Describe the morphology of the erythrocytes.
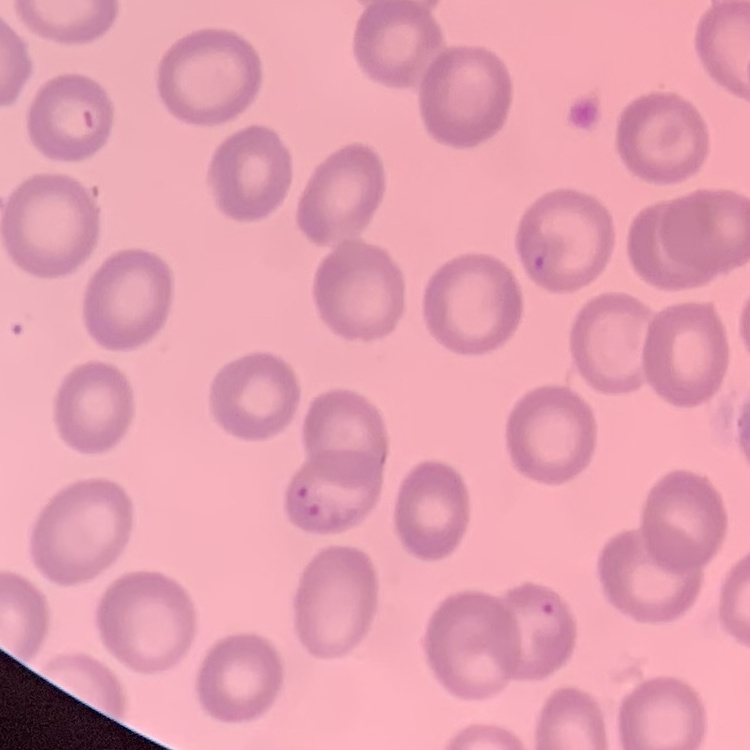
They show no rouleaux formation.

Thin blood smear. One tile cut from a larger photomicrograph. Stained with either Field's or Giemsa.